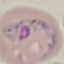
Result: malaria parasites detected. Giemsa stain. Photographed with a smartphone camera at the microscope eyepiece. Automatically extracted cell patch, resized to 64 × 64 pixels. Thin blood film.